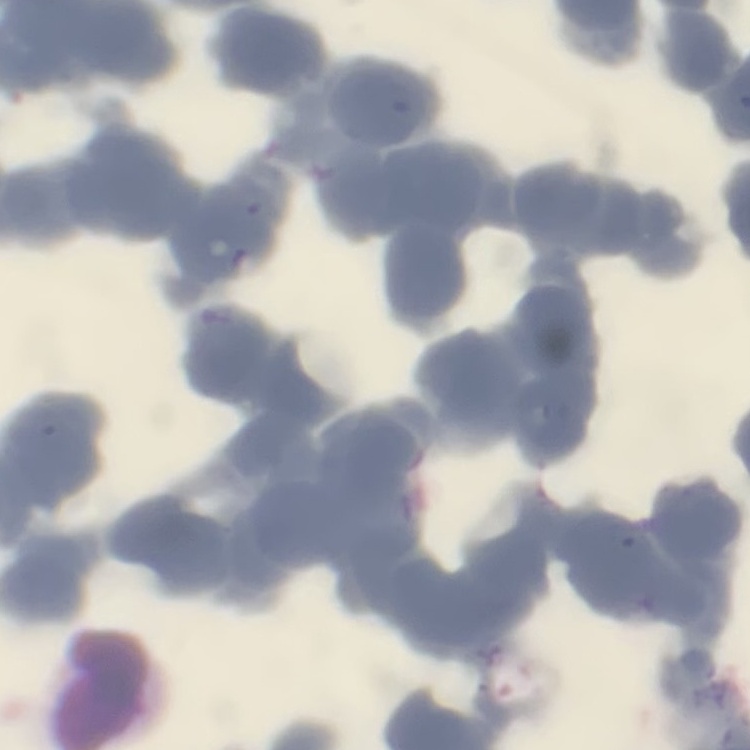
{
  "erythrocyte_morphology": "rouleaux formation",
  "image_type": "one tile cut from a larger photomicrograph",
  "stain": "Field's or Giemsa",
  "preparation": "thin blood film"
}